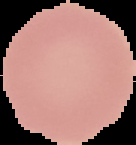
Segmented cell region on a black background. Image is 136×145 pixels. From a thin blood smear. Malaria status: uninfected.